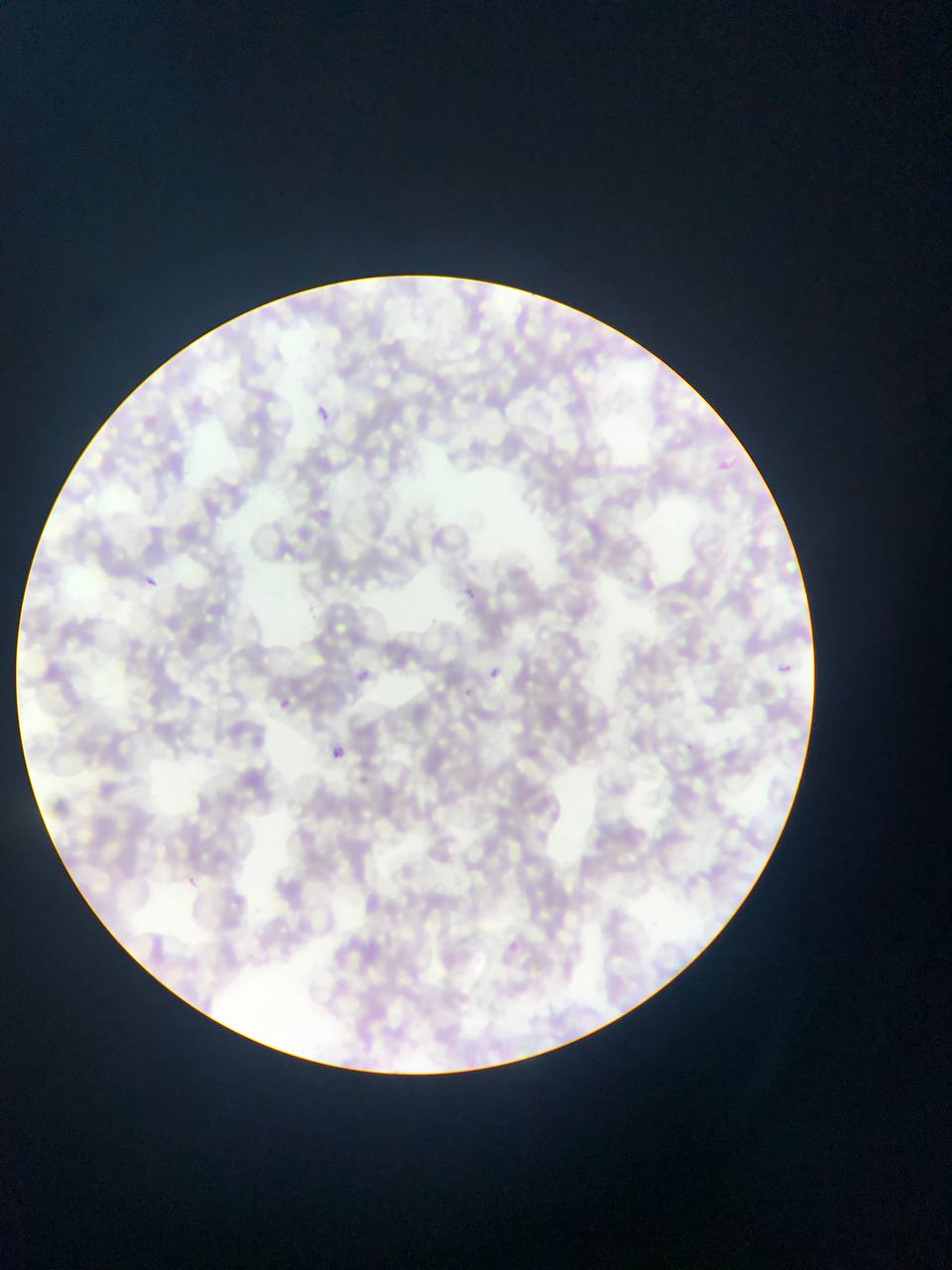
{
  "preparation": "thin blood film",
  "capture": "mobile-phone photograph through a microscope",
  "plasmodium_parasite_locations": "approximate bounding boxes as [left, top, right, bottom] in pixels: [312, 404, 342, 431], [712, 456, 737, 478], [142, 575, 158, 590], [460, 585, 479, 603], [776, 662, 793, 678], [350, 664, 374, 687], [483, 665, 506, 685], [273, 695, 296, 716], [329, 745, 345, 761], [179, 871, 203, 893]",
  "country": "Ghana",
  "image_size": "952×1270 pixels",
  "field_of_view": "single"
}